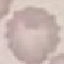
Summary:
  - Malaria status: uninfected
  - Preparation: thin blood film
  - Image type: automatically extracted cell patch, resized to 64 × 64 pixels
  - Capture: smartphone through the microscope eyepiece
  - Stain: Giemsa